State which cell type is depicted.
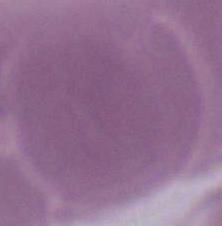
This is an erythrocyte.

modality = micrograph
magnification = 1000x